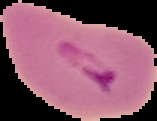

Result: malaria parasites detected. The area outside the segmented cell region is set to black. Image is 157×121 pixels. From a thin blood smear.